Assess this cell for malaria.
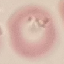

It is parasitized.

Giemsa-stained preparation. Cell patch, automatically extracted from a larger field of view and resized to 64 × 64 pixels. Thin smear of blood. Acquired by smartphone through the microscope eyepiece.